Locate every blood parasite and identify its species.
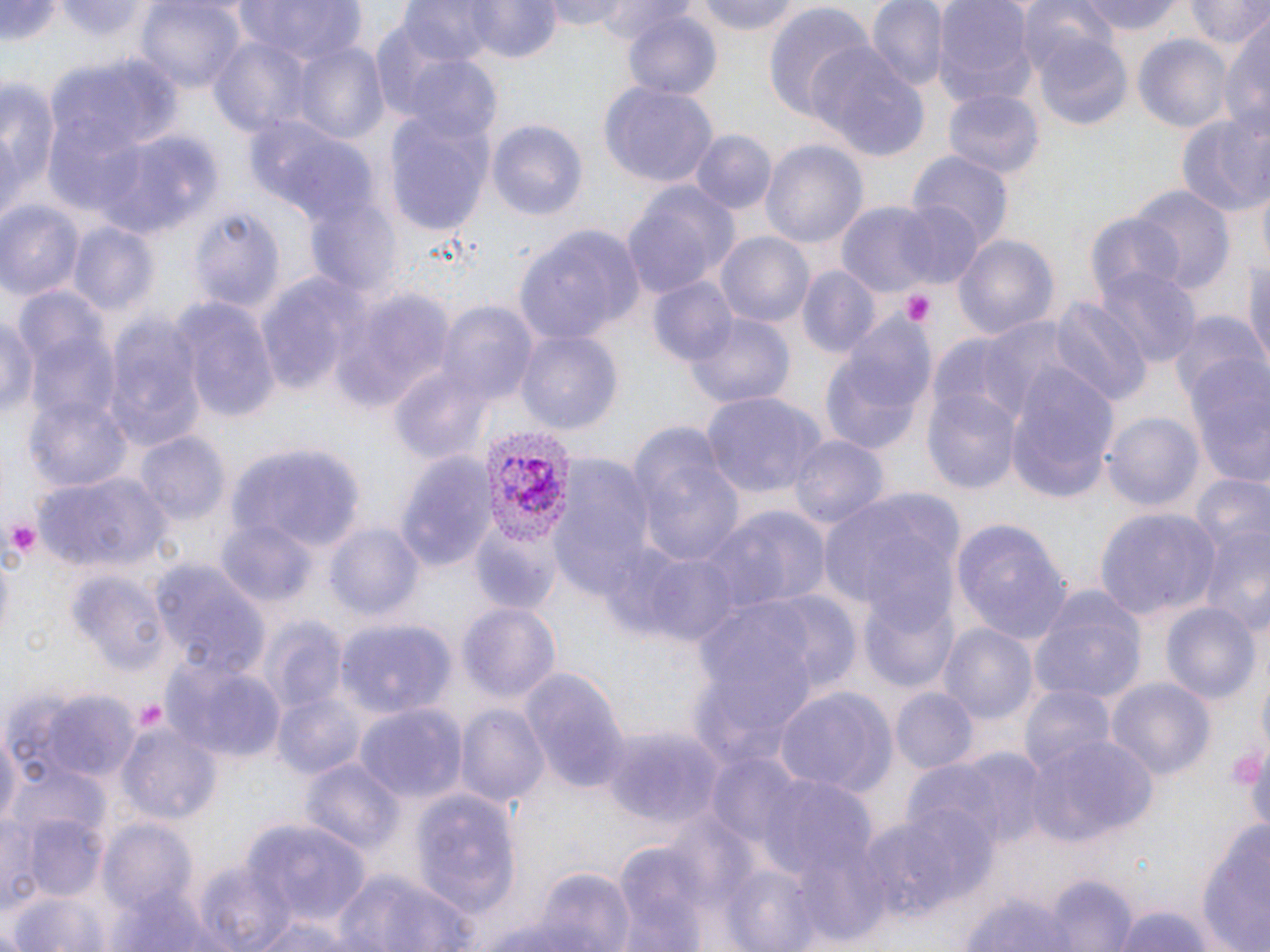

Approximate bounding boxes as (x1,y1)-(x2,y2) corner pairs in pixels.
Plasmodium vivax-infected red blood cells: (479,425)-(580,549).
No Plasmodium falciparum, Plasmodium ovale, Plasmodium malariae, Babesia divergens, or Trypanosoma brucei observed.

slide-level diagnosis = Plasmodium vivax
stain = May-Grünwald-Giemsa
platelet locations = approximate bounding boxes as (x1,y1)-(x2,y2) corner pairs in pixels: (900,289)-(936,327), (2,516)-(38,565), (130,698)-(170,736), (1233,751)-(1267,785)
modality = optical microscopy
preparation = thin blood smear
magnification = 1000x
image size = 1270×952 pixels
field of view = one of a larger specimen
uninfected red blood cell locations = approximate bounding boxes as (x1,y1)-(x2,y2) corner pairs in pixels: (2,0)-(64,46), (59,0)-(152,42), (232,0)-(368,68), (547,0)-(639,32), (590,0)-(693,44), (692,0)-(806,36), (866,0)-(948,95), (932,0)-(1037,111), (1016,0)-(1122,79), (1081,0)-(1186,36), (1188,0)-(1267,51), (136,1)-(244,94), (468,1)-(560,63), (397,2)-(508,66), (763,5)-(876,123), (622,9)-(722,102), (1218,19)-(1270,136), (1032,31)-(1134,130), (1134,32)-(1233,134), (208,35)-(316,141), (293,39)-(389,146), (809,46)-(929,161), (49,55)-(182,164), (405,58)-(503,147), (0,73)-(60,220), (599,79)-(718,188), (944,90)-(1042,182), (1176,113)-(1267,220), (384,114)-(494,237), (245,116)-(376,228), (488,120)-(589,225), (689,130)-(774,215), (91,131)-(216,241), (762,141)-(868,247), (907,151)-(1012,254), (622,182)-(740,299), (1129,185)-(1234,296), (303,191)-(400,299), (894,199)-(987,290), (0,200)-(84,301), (834,202)-(952,299), (188,207)-(284,316), (1084,211)-(1182,308), (70,223)-(157,314), (516,223)-(645,344), (717,232)-(814,329), (954,233)-(1060,341), (1242,252)-(1270,375), (1095,264)-(1201,371), (798,267)-(878,359), (255,274)-(366,396), (646,276)-(738,368), (327,289)-(451,410), (173,297)-(280,421), (1049,298)-(1150,410), (437,302)-(540,409), (1168,309)-(1265,414), (1,310)-(38,425), (685,311)-(795,408), (99,315)-(206,455), (822,317)-(937,453), (516,329)-(621,434), (1182,360)-(1270,487), (1003,364)-(1118,507), (389,369)-(493,466), (925,389)-(1022,496), (24,390)-(134,495), (704,391)-(826,501), (1103,408)-(1203,511), (627,424)-(744,570), (136,432)-(229,527), (788,435)-(887,534), (228,442)-(359,556), (392,453)-(497,573), (550,453)-(662,599), (34,472)-(170,572), (1184,476)-(1270,624), (818,487)-(965,626), (701,507)-(831,618), (1095,508)-(1220,619), (470,516)-(560,612), (217,518)-(317,608), (950,519)-(1072,645), (324,522)-(425,621), (617,547)-(747,647), (152,560)-(269,677), (71,570)-(169,675), (1027,581)-(1149,709), (737,589)-(864,695), (864,598)-(959,694), (458,601)-(562,705), (1161,602)-(1260,705), (260,618)-(347,717), (338,618)-(458,717), (939,622)-(1038,728), (163,659)-(284,763), (518,664)-(627,795), (1106,679)-(1216,778), (1021,683)-(1116,779), (772,686)-(895,801), (36,688)-(140,781), (891,688)-(976,773), (275,694)-(368,780), (355,701)-(467,803), (456,705)-(549,810), (0,720)-(21,829), (119,722)-(222,827), (599,722)-(724,828), (1025,736)-(1159,846), (942,749)-(1051,849), (299,755)-(405,857), (7,766)-(107,841), (745,768)-(878,880), (409,793)-(521,919), (896,802)-(998,906), (853,807)-(979,932), (1193,814)-(1270,952), (2,815)-(42,914), (24,816)-(111,902), (101,820)-(200,917), (246,822)-(369,926), (615,845)-(712,950), (720,863)-(825,952), (329,868)-(479,952), (526,870)-(633,949), (1046,873)-(1132,951), (957,890)-(1081,950), (9,895)-(106,952), (1105,904)-(1220,952), (474,910)-(605,952)